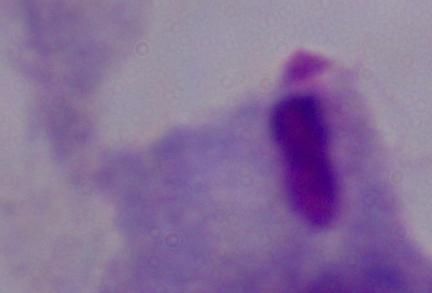

Summary:
  - Magnification: 1000x
  - Identification: trichomonad
  - Modality: micrograph